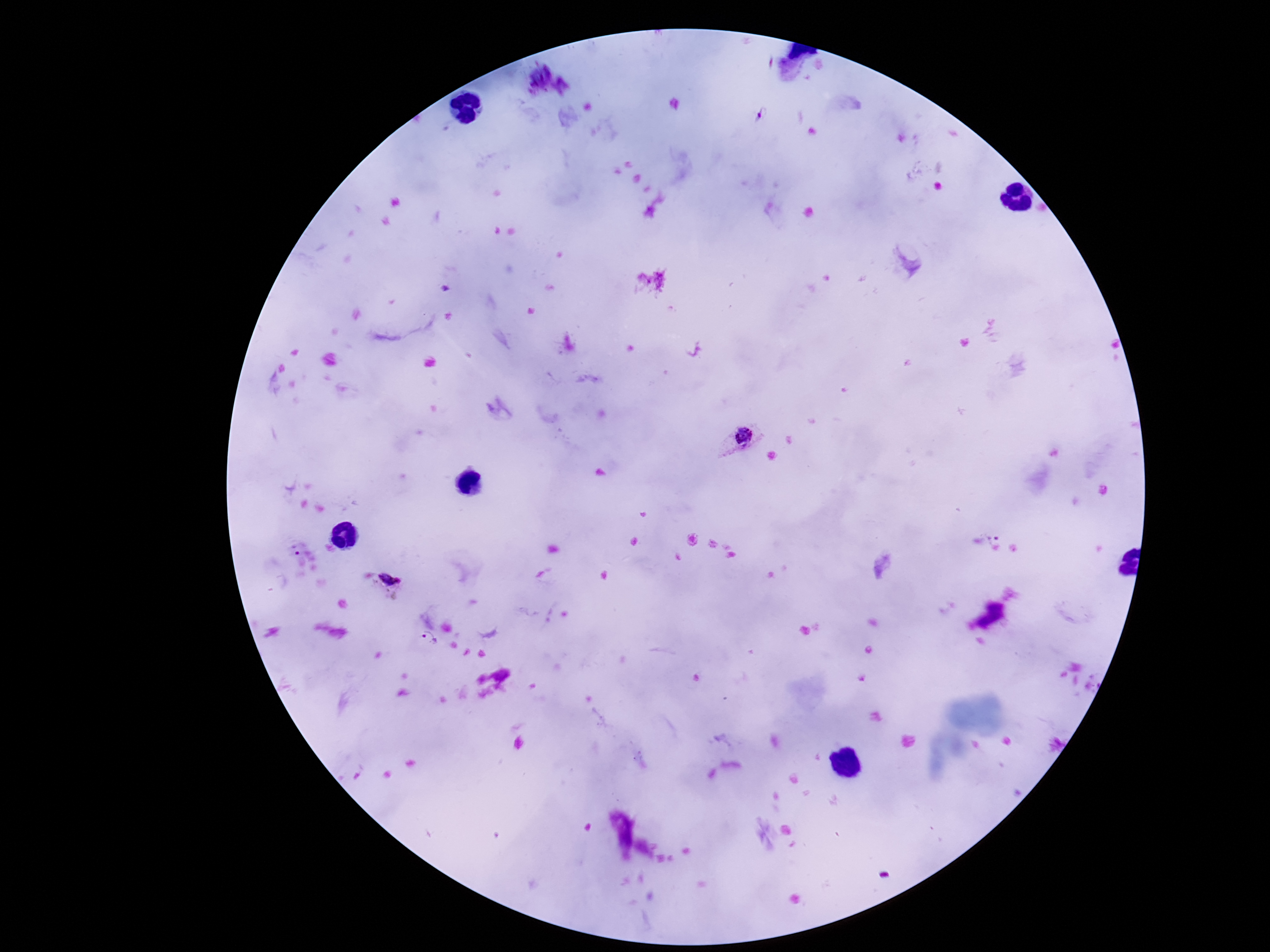
Approximate centers as [x, y] in pixels.
Summary:
  - Plasmodium parasite locations: [763, 116], [740, 438], [998, 537], [296, 553], [391, 578], [429, 639]
  - Preparation: thick blood film
  - Capture: smartphone camera through the microscope eyepiece
  - Patient malaria status: infected
  - Field of view: one from this slide
  - Magnification: 100x
  - Stain: Giemsa
  - Image size: 1270×952 pixels